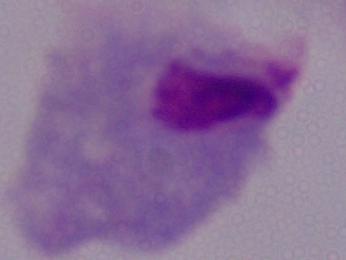
{
  "identification": "trichomonad",
  "magnification": "1000x",
  "modality": "micrograph"
}